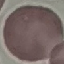
{
  "result": "negative for malaria parasites",
  "image_type": "cell patch, automatically extracted from a larger field of view and resized to 64 × 64 pixels",
  "preparation": "thin smear",
  "capture": "smartphone camera at the microscope eyepiece",
  "stain": "Giemsa"
}